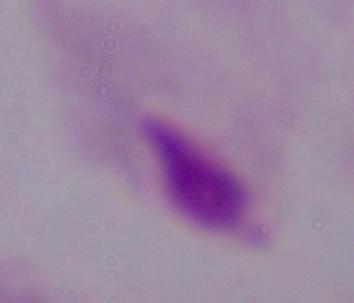
Summary:
  - Modality: micrograph
  - Identification: trichomonad
  - Magnification: 1000x